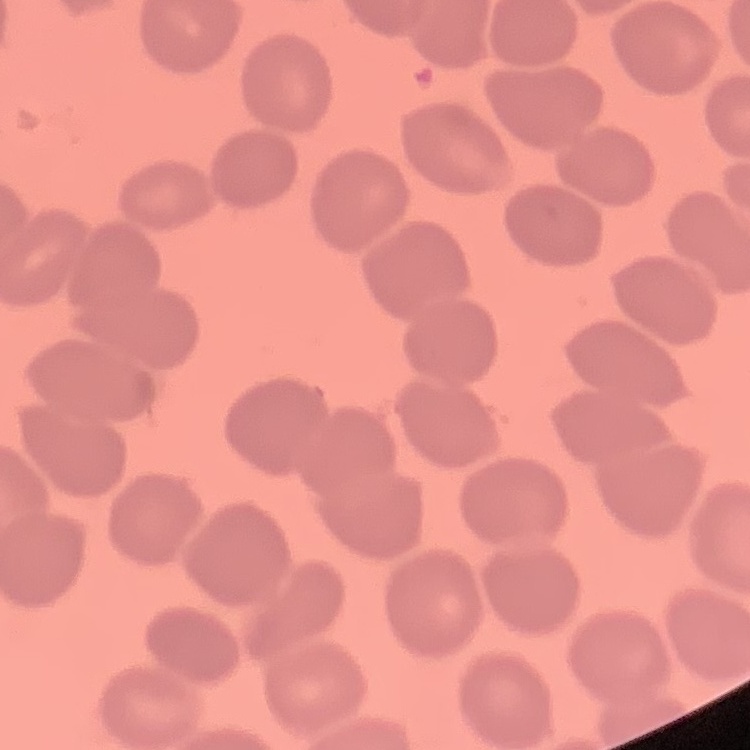
The erythrocytes show no rouleaux formation. Thin peripheral smear. Field's or Giemsa stain. One tile cut from a larger photomicrograph.